Locate and identify every blood parasite.
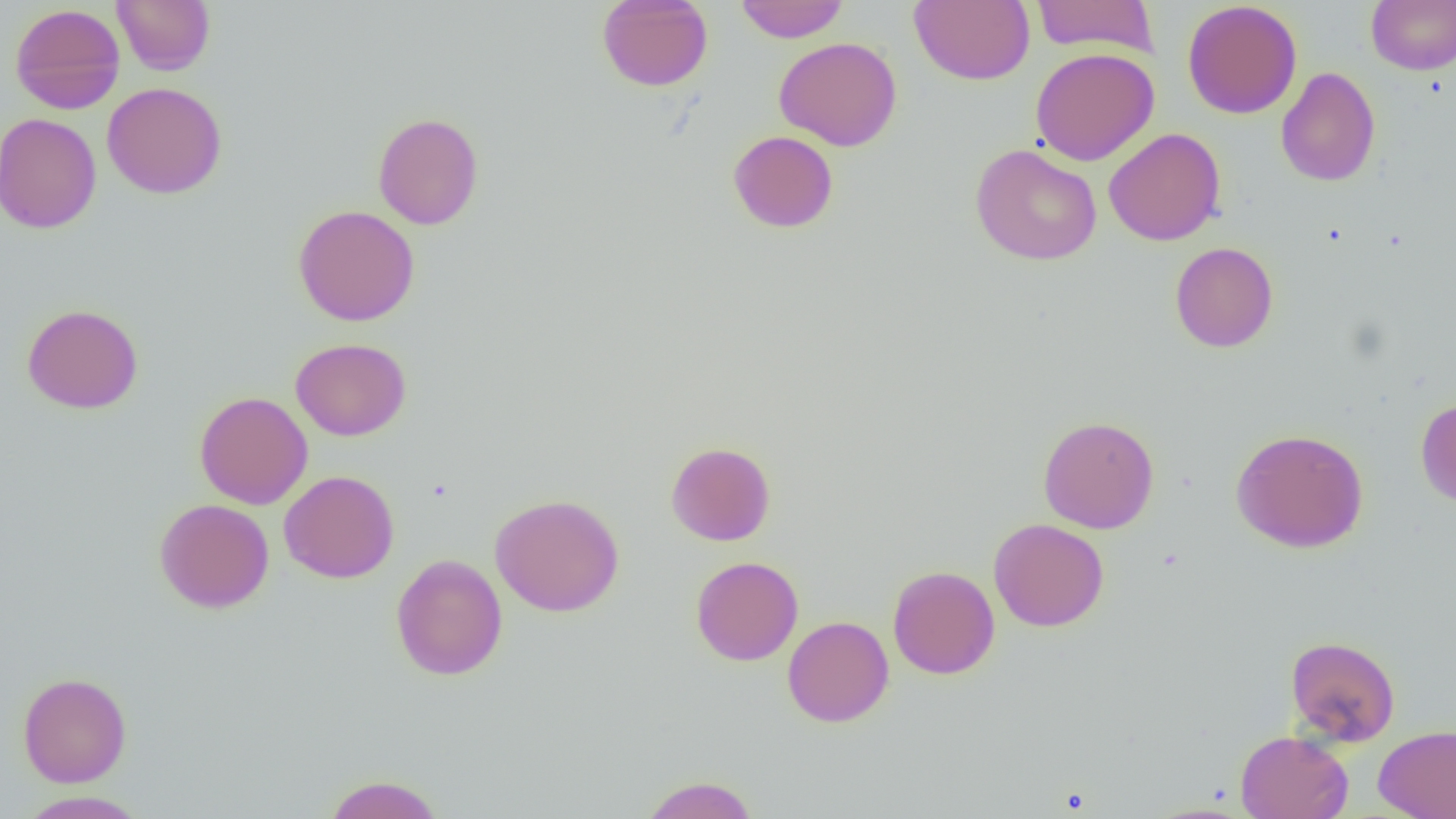
No blood parasites observed.

slide-level diagnosis = negative for blood parasites
magnification = 1000x
image size = 1456×819 pixels
field of view = one of a larger specimen
modality = light microscopy
preparation = thin blood film
uninfected red blood cell locations = approximate bounding boxes as (x1,y1)-(x2,y2) corner pairs in pixels: (112,0)-(215,75), (596,0)-(714,91), (735,0)-(848,43), (909,0)-(1035,85), (1030,0)-(1159,57), (1366,0)-(1456,75), (1182,1)-(1302,119), (10,3)-(126,114), (773,36)-(903,152), (1030,48)-(1159,166), (1276,66)-(1380,186), (101,82)-(227,199), (0,112)-(102,234), (373,112)-(484,230), (1103,128)-(1226,246), (728,130)-(838,233), (970,143)-(1102,266), (293,205)-(420,326), (1170,241)-(1278,352), (22,303)-(144,414), (290,338)-(411,441), (194,391)-(313,509), (1416,398)-(1456,507), (1038,415)-(1159,534), (1230,428)-(1369,552), (665,441)-(776,546), (279,470)-(399,584), (489,493)-(625,617), (154,498)-(274,613), (988,518)-(1109,632), (390,553)-(507,681), (690,555)-(803,666), (887,565)-(1000,680), (782,615)-(894,727), (1285,635)-(1400,747), (18,672)-(131,787), (1373,724)-(1456,819), (1235,730)-(1354,819), (323,773)-(444,819), (640,774)-(759,819), (16,790)-(149,818), (1141,802)-(1255,819)